Locate every blood parasite and identify its species.
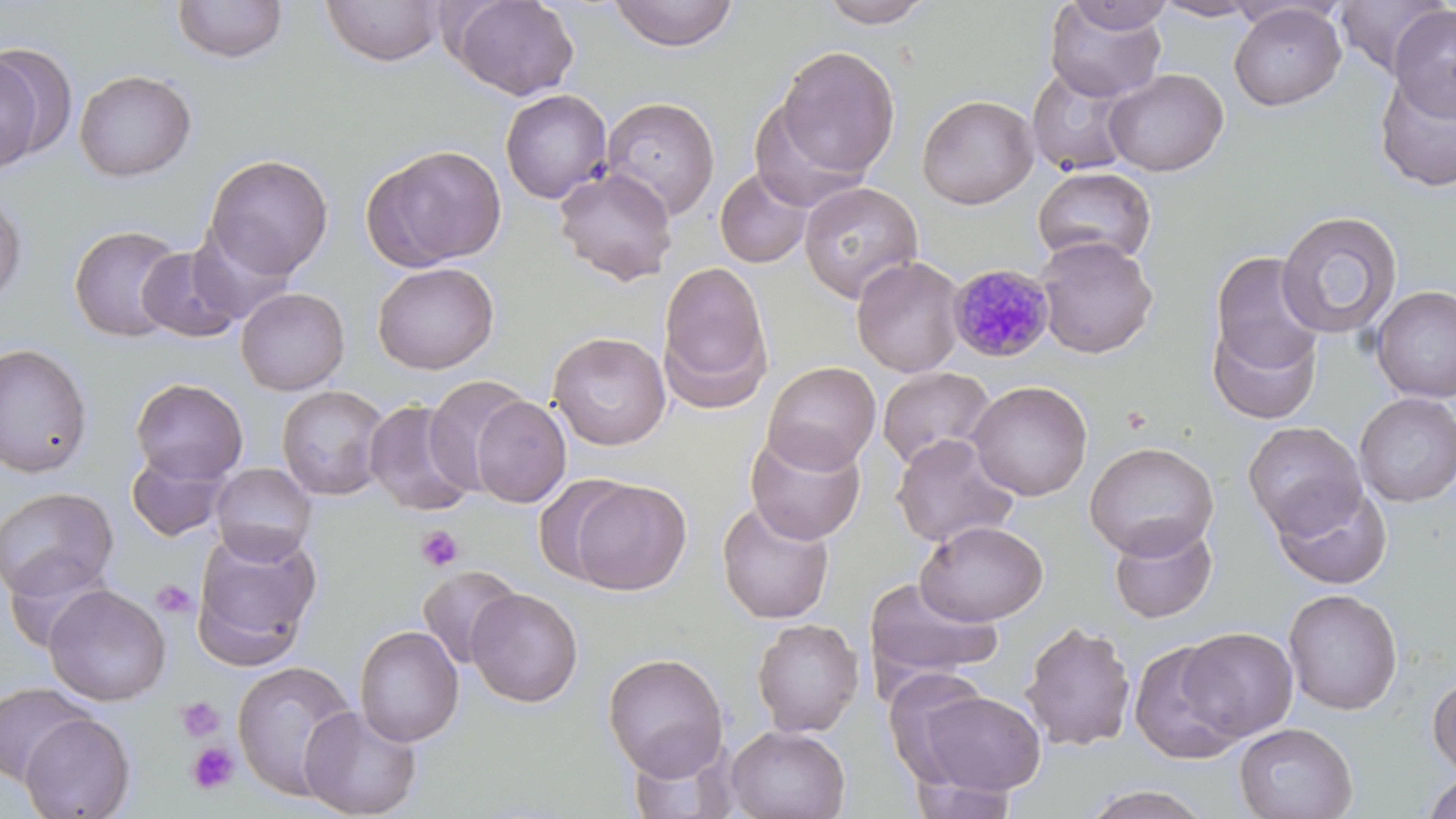
Approximate bounding boxes as (x1, y1, x2, y2) in pixels.
Plasmodium malariae-infected red blood cells: (947, 263, 1054, 362).
No Plasmodium falciparum, Plasmodium ovale, Plasmodium vivax, Babesia divergens, or Trypanosoma brucei observed.

slide-level diagnosis = Plasmodium malariae
image size = 1456×819 pixels
modality = optical microscopy
stain = May-Grünwald-Giemsa
platelet locations = approximate bounding boxes as (x1, y1, x2, y2) in pixels: (1121, 405, 1153, 435), (416, 525, 463, 571), (150, 579, 198, 620), (175, 696, 225, 742), (186, 742, 239, 795)
magnification = 1000x
field of view = single
preparation = thin blood film
uninfected red blood cell locations = approximate bounding boxes as (x1, y1, x2, y2) in pixels: (171, 0, 290, 65), (449, 0, 579, 100), (814, 0, 939, 28), (1153, 0, 1264, 21), (1334, 0, 1451, 77), (321, 1, 446, 67), (606, 1, 740, 52), (1044, 1, 1168, 102), (1062, 1, 1177, 34), (1229, 4, 1346, 111), (1387, 6, 1456, 121), (775, 45, 901, 179), (0, 50, 48, 171), (1026, 65, 1141, 178), (74, 69, 197, 182), (1103, 69, 1228, 176), (1373, 69, 1456, 192), (500, 89, 613, 204), (917, 94, 1039, 210), (600, 97, 721, 220), (749, 100, 867, 212), (363, 144, 508, 270), (203, 153, 334, 280), (1032, 165, 1157, 267), (554, 166, 677, 286), (714, 167, 813, 269), (799, 182, 923, 303), (0, 189, 28, 306), (1276, 210, 1403, 340), (68, 224, 186, 342), (187, 225, 298, 324), (1035, 236, 1159, 358), (136, 246, 245, 342), (1208, 251, 1325, 379), (851, 255, 966, 377), (657, 260, 774, 410), (372, 262, 499, 374), (1370, 285, 1456, 403), (235, 287, 350, 395), (1207, 312, 1324, 426), (548, 332, 671, 450), (0, 342, 94, 478), (761, 361, 881, 474), (876, 366, 996, 471), (424, 376, 535, 497), (130, 377, 249, 485), (967, 380, 1093, 501), (276, 385, 391, 501), (1354, 393, 1456, 507), (468, 395, 571, 508), (363, 398, 479, 517), (1243, 421, 1366, 536), (744, 428, 866, 545), (891, 433, 1019, 548), (1084, 441, 1219, 560), (126, 451, 230, 542), (210, 462, 317, 563), (567, 478, 692, 595), (1272, 481, 1393, 590), (0, 486, 119, 603), (716, 500, 835, 624), (915, 520, 1048, 626), (1107, 520, 1219, 624), (192, 527, 323, 667), (417, 564, 522, 669), (863, 577, 1003, 690), (43, 584, 171, 706), (465, 588, 584, 708), (1283, 588, 1403, 714), (751, 618, 864, 737), (1019, 621, 1136, 751), (354, 625, 464, 747), (1177, 627, 1299, 741), (1128, 640, 1245, 764), (603, 651, 729, 780), (232, 660, 359, 800), (1428, 673, 1456, 778), (0, 682, 94, 784), (910, 689, 1048, 796), (299, 704, 423, 818), (19, 712, 136, 818), (1233, 722, 1358, 819), (725, 725, 851, 819), (624, 737, 737, 819), (1422, 773, 1456, 819), (905, 776, 1022, 818), (1078, 785, 1215, 819)